Outline each blood parasite and name the species.
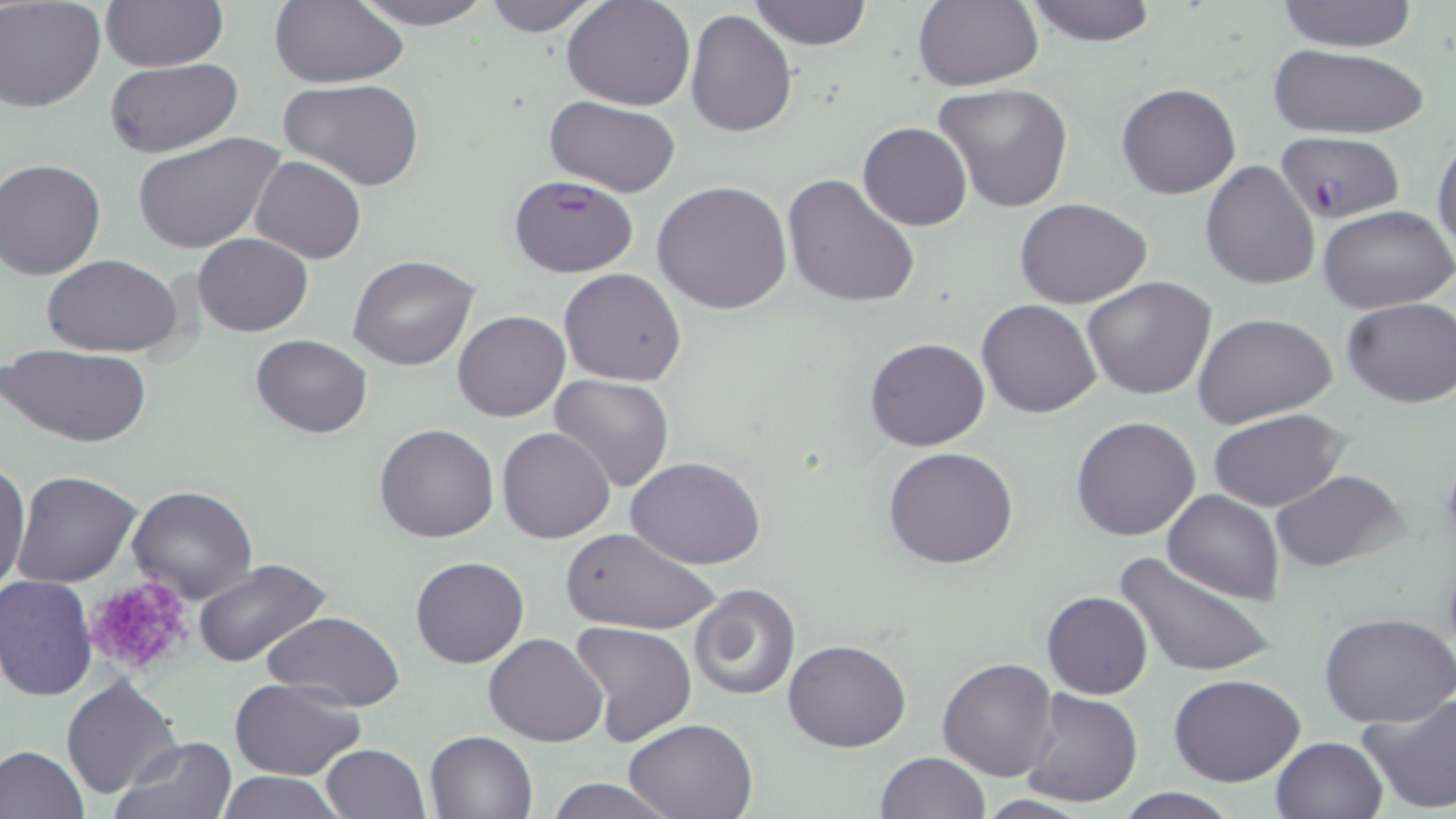

Approximate bounding boxes as [x1, y1, x2, y2] in pixels.
Plasmodium falciparum-infected red blood cells: [1276, 133, 1405, 224], [508, 173, 639, 278].
No Plasmodium ovale, Plasmodium malariae, Plasmodium vivax, Babesia divergens, or Trypanosoma brucei observed.

Summary:
  - Uninfected red blood cell locations: [100, 0, 227, 70], [269, 0, 408, 87], [346, 0, 500, 29], [478, 0, 607, 36], [562, 0, 695, 110], [748, 0, 873, 50], [912, 0, 1042, 91], [1021, 0, 1161, 45], [1272, 0, 1421, 51], [1, 1, 106, 110], [685, 8, 797, 137], [1266, 43, 1431, 140], [103, 58, 242, 158], [282, 78, 425, 190], [933, 82, 1076, 214], [1116, 82, 1240, 199], [543, 96, 681, 198], [858, 122, 970, 231], [133, 131, 285, 257], [1432, 134, 1456, 256], [251, 155, 367, 265], [1, 160, 105, 280], [1200, 161, 1320, 291], [781, 172, 920, 308], [651, 181, 792, 316], [1014, 198, 1152, 308], [1318, 204, 1455, 313], [195, 233, 311, 336], [43, 253, 186, 356], [348, 253, 479, 371], [559, 268, 688, 386], [1081, 276, 1217, 399], [1341, 296, 1456, 408], [977, 299, 1102, 418], [453, 311, 569, 423], [1192, 311, 1338, 427], [251, 333, 374, 437], [864, 337, 990, 452], [6, 344, 150, 447], [549, 374, 676, 493], [1207, 408, 1352, 513], [1071, 415, 1201, 541], [374, 424, 499, 542], [497, 427, 616, 545], [883, 445, 1020, 570], [627, 457, 767, 570], [0, 461, 30, 593], [1270, 469, 1409, 573], [11, 471, 142, 587], [126, 487, 257, 604], [1162, 489, 1285, 603], [560, 528, 718, 637], [1115, 551, 1275, 681], [409, 556, 529, 668], [192, 557, 335, 672], [0, 573, 98, 701], [690, 582, 801, 702], [1041, 590, 1151, 699], [262, 609, 407, 712], [1320, 611, 1456, 728], [569, 622, 697, 747], [483, 634, 608, 747], [783, 638, 911, 752], [937, 657, 1059, 782], [61, 674, 181, 799], [1169, 675, 1307, 788], [230, 678, 366, 780], [1020, 688, 1142, 808], [1356, 690, 1456, 813], [623, 718, 758, 819], [424, 730, 538, 819], [112, 736, 238, 818], [1271, 736, 1389, 819], [319, 743, 431, 819], [0, 745, 88, 817], [874, 751, 990, 818], [215, 771, 344, 818], [540, 777, 679, 818], [1108, 790, 1245, 819]
  - Platelet locations: [83, 576, 194, 677]
  - Slide-level diagnosis: Plasmodium falciparum
  - Preparation: thin blood film
  - Image size: 1456×819 pixels
  - Stain: May-Grünwald-Giemsa
  - Modality: optical microscopy
  - Magnification: 1000x
  - Field of view: one of a larger specimen